Assess this cell for malaria.
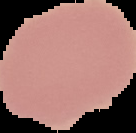
It is uninfected.

Image is 136×133 pixels. From a thin blood smear. Segmented cell region on a black background.